State which parasite is depicted.
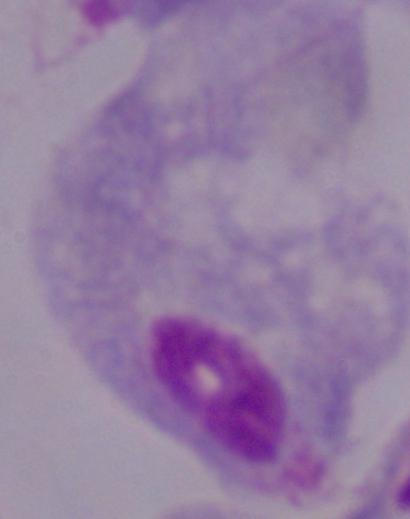

A trichomonad.

Summary:
  - Magnification: 1000x
  - Modality: photomicrograph